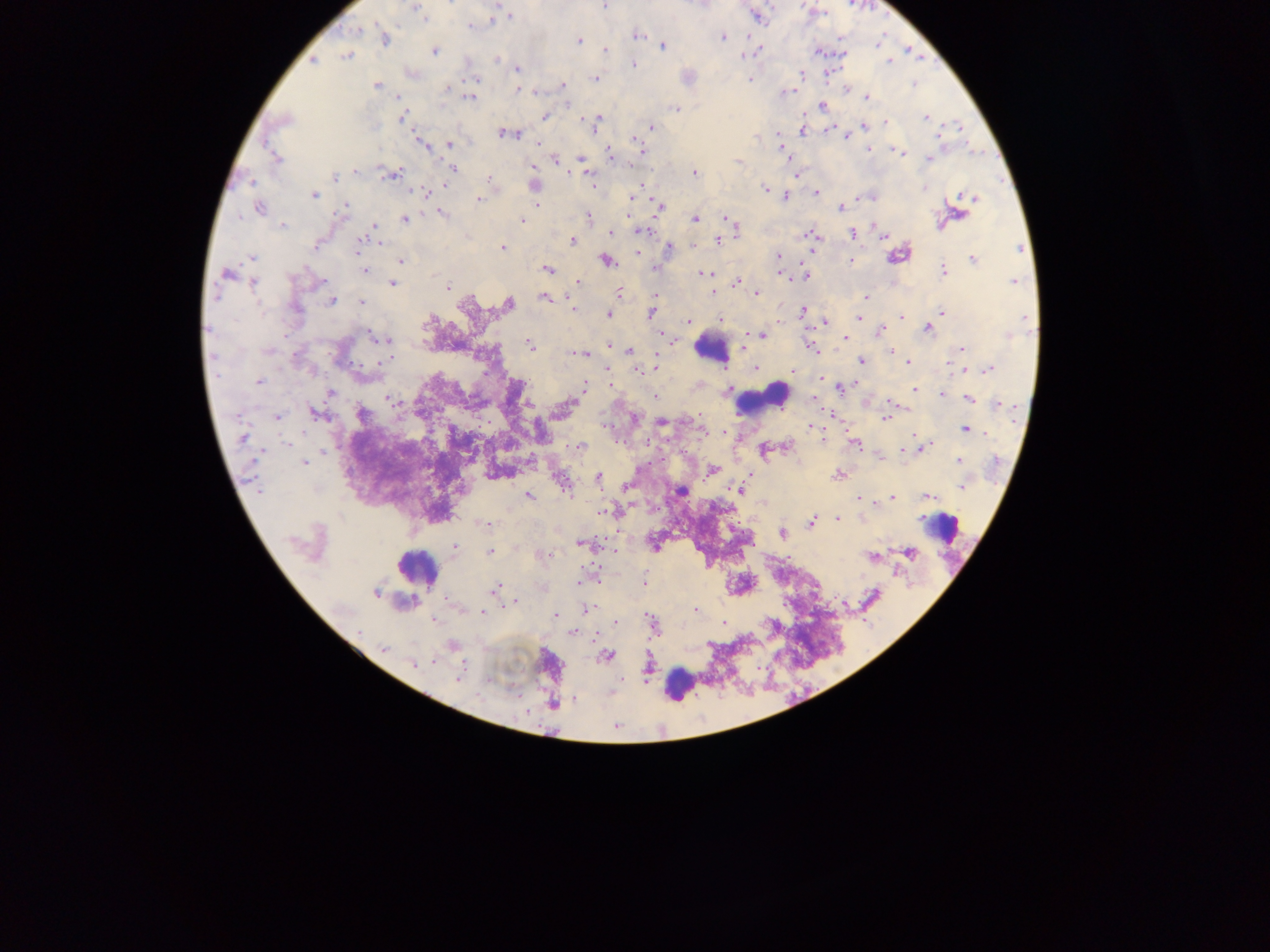
{
  "leukocyte_locations": "approximate centers as [x, y] in pixels: [711, 348], [765, 399], [941, 527], [417, 567], [679, 684]",
  "image_size": "1270×952 pixels",
  "malaria_parasite_locations": "approximate centers as [x, y] in pixels: [604, 6], [416, 8], [509, 17], [758, 17], [470, 25], [356, 30], [636, 35], [722, 37], [385, 38], [579, 40], [663, 46], [606, 50], [434, 51], [818, 52], [347, 56], [497, 59], [314, 62], [888, 62], [634, 65], [518, 69], [687, 76], [596, 78], [749, 80], [473, 81], [376, 85], [562, 86], [449, 88], [519, 89], [847, 90], [785, 93], [868, 96], [471, 97], [823, 106], [676, 109], [545, 116], [402, 117], [926, 118], [288, 119], [887, 122], [593, 123], [863, 126], [651, 128], [505, 134], [844, 135], [756, 137], [421, 143], [450, 144], [639, 147], [870, 149], [784, 151], [897, 152], [611, 155], [275, 158], [581, 159], [929, 159], [738, 160], [452, 169], [584, 170], [695, 173], [390, 175], [335, 177], [489, 179], [252, 182], [534, 185], [765, 188], [924, 188], [816, 191], [422, 192], [313, 194], [785, 196], [971, 198], [478, 199], [660, 206], [258, 208], [345, 208], [841, 208], [442, 214], [959, 214], [588, 217], [405, 219], [695, 219], [728, 219], [522, 220], [941, 222], [731, 223], [283, 226], [374, 226], [641, 231], [612, 232], [852, 234], [883, 234], [810, 235], [717, 240], [572, 241], [364, 242], [316, 246], [501, 247], [670, 248], [1019, 248], [897, 254], [778, 256], [252, 257], [851, 260], [973, 260], [401, 261], [607, 261], [548, 269], [654, 269], [364, 270], [943, 271], [227, 273], [704, 273], [806, 275], [254, 282], [578, 282], [1014, 282], [736, 283], [392, 284], [447, 286], [619, 292], [713, 293], [757, 293], [546, 297], [865, 297], [331, 301], [362, 302], [507, 305], [573, 307], [295, 309], [941, 311], [803, 312], [651, 313], [608, 314], [901, 317], [1026, 318], [720, 319], [858, 319], [688, 321], [826, 321], [928, 329], [880, 332], [762, 335], [1010, 335], [844, 338], [382, 339], [530, 346], [610, 346], [811, 348], [961, 349], [630, 350], [892, 351], [580, 354], [861, 363], [908, 363], [956, 369], [639, 370], [989, 370], [792, 371], [821, 379], [258, 381], [584, 385], [841, 388], [915, 390], [728, 391], [331, 393], [943, 395], [654, 396], [968, 399], [391, 400], [1000, 404], [565, 407], [318, 414], [361, 415], [277, 417], [886, 417], [661, 422], [810, 427], [966, 429], [244, 436], [855, 444], [580, 446], [923, 448], [765, 450], [903, 451], [959, 460], [304, 462], [711, 470], [837, 475], [599, 478], [561, 481], [962, 485], [739, 490], [680, 492], [528, 495], [893, 497], [930, 497], [858, 498], [610, 512], [837, 518], [487, 523], [811, 523], [783, 534], [581, 544], [454, 547], [490, 551], [910, 553], [872, 557], [645, 582], [495, 588], [375, 593], [514, 601], [587, 609], [695, 610], [482, 612], [556, 616], [724, 622], [652, 623], [573, 633], [452, 645], [384, 649], [606, 655], [414, 663], [458, 676], [554, 704]",
  "field_of_view": "single",
  "preparation": "thick blood smear",
  "capture": "mobile-phone photograph through a microscope",
  "country": "Ghana"
}